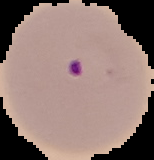 Segmented cell region on a black background. Result: Plasmodium parasites identified. From a thin blood smear. Image is 154×160 pixels.